Evaluate for parasitized red blood cells.
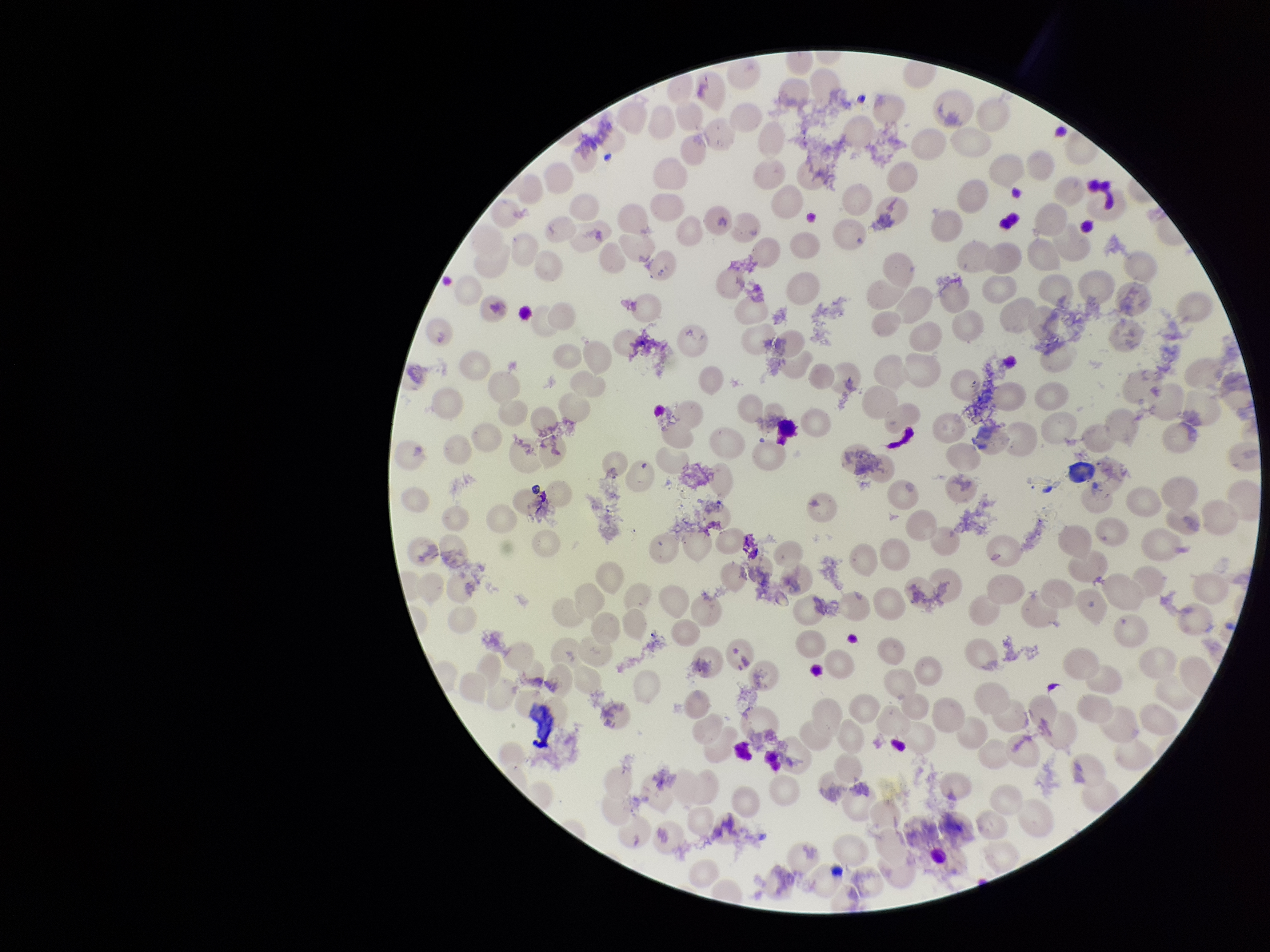

None identified.

Preparation: thin blood smear. Image is 1270×952 pixels. One field from this slide. Parasitized red blood cell count: 0. Smartphone photograph taken through the eyepiece of a microscope. Patient malaria status: infected. Species reported for this patient: Plasmodium vivax. Stained with Giemsa. Red blood cell count: 187.